Comment on the morphology of the erythrocytes.
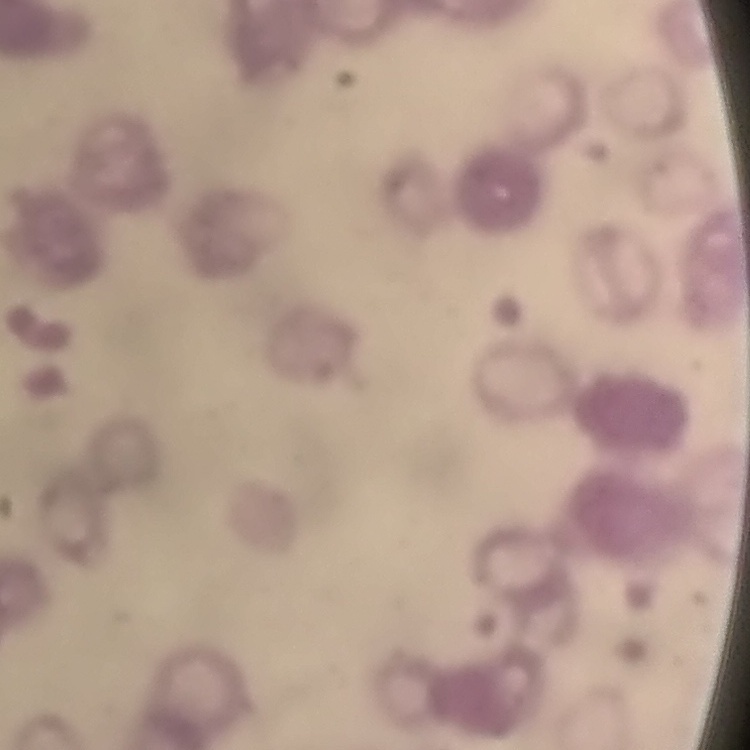

Rouleaux formation.

Summary:
  - Stain: Field's or Giemsa
  - Image type: one tile cut from a larger photomicrograph
  - Preparation: thin blood smear